Report the malaria status of this cell.
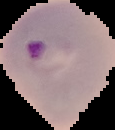
Parasitized.

image type = cell region segmented out of the field of view; surrounding area masked to black
preparation = thin blood smear
image size = 115×130 pixels